Classify this cell by malaria status.
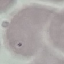

Uninfected.

Giemsa-stained preparation. Acquired by smartphone through the microscope eyepiece. Thin smear of blood. Cell patch, automatically extracted from a larger field of view and resized to 64 × 64 pixels.